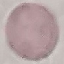

Result: negative for malaria parasites. Thin smear of blood. Cell patch, automatically extracted from a larger field of view and resized to 64 × 64 pixels. Giemsa-stained preparation. Photographed with a smartphone camera at the microscope eyepiece.